Locate every Plasmodium malariae-infected red blood cell.
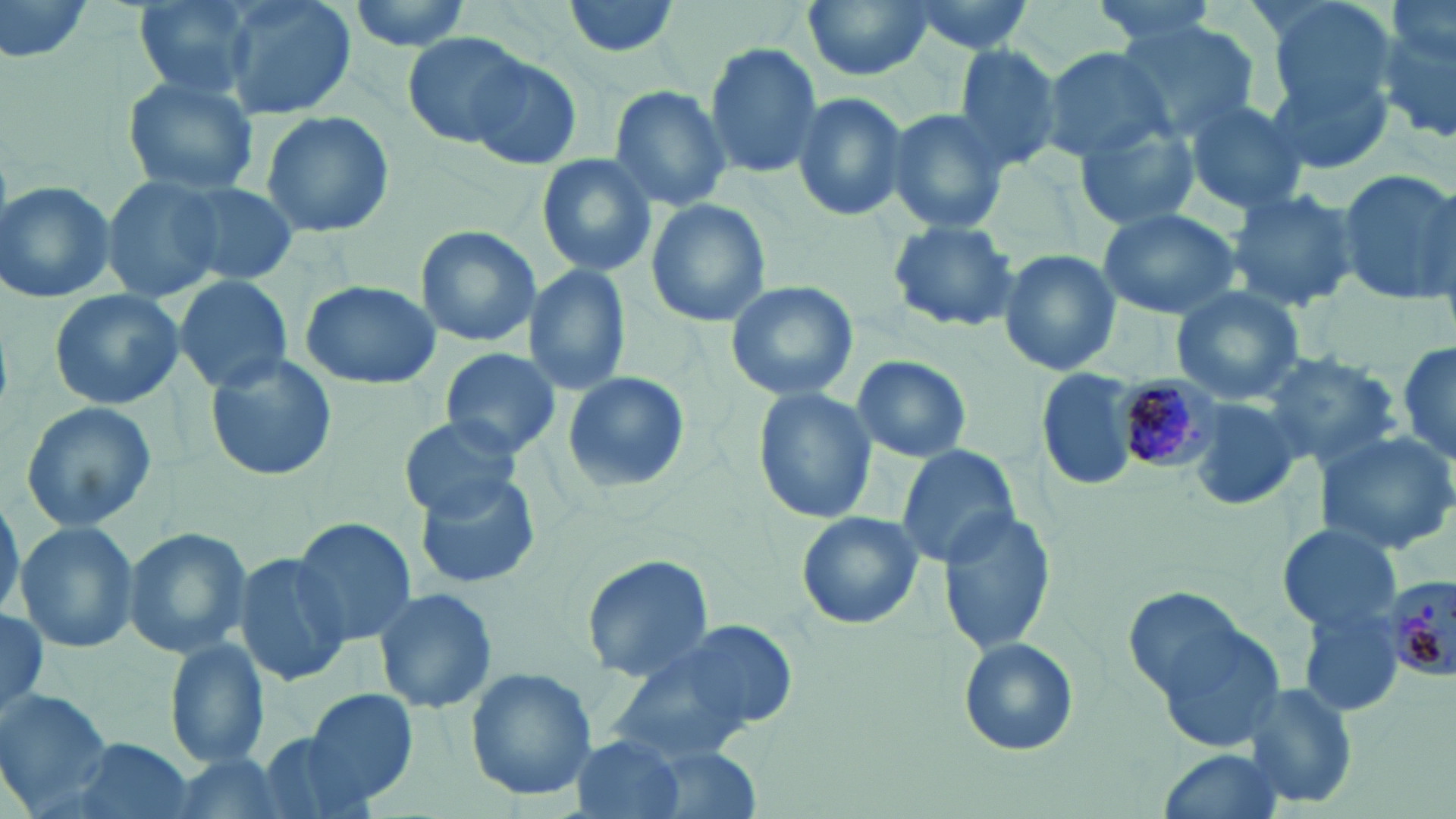

Approximate bounding boxes as named x1/y1/x2/y2 corners in pixels.
Plasmodium malariae-infected red blood cells: (x1=1106, y1=373, x2=1225, y2=472), (x1=1385, y1=575, x2=1456, y2=684).

slide-level diagnosis = Plasmodium malariae
stain = May-Grünwald-Giemsa
modality = optical microscopy
image size = 1456×819 pixels
preparation = thin blood smear
uninfected red blood cell locations = approximate bounding boxes as named x1/y1/x2/y2 corners in pixels: (x1=0, y1=0, x2=106, y2=65), (x1=130, y1=0, x2=257, y2=96), (x1=220, y1=0, x2=355, y2=121), (x1=345, y1=0, x2=479, y2=52), (x1=561, y1=0, x2=685, y2=58), (x1=802, y1=0, x2=935, y2=82), (x1=895, y1=0, x2=1039, y2=57), (x1=1086, y1=0, x2=1224, y2=50), (x1=1377, y1=0, x2=1456, y2=147), (x1=1261, y1=13, x2=1397, y2=173), (x1=1118, y1=21, x2=1261, y2=142), (x1=403, y1=31, x2=529, y2=147), (x1=702, y1=41, x2=825, y2=180), (x1=948, y1=41, x2=1065, y2=176), (x1=1040, y1=46, x2=1175, y2=162), (x1=464, y1=53, x2=585, y2=172), (x1=120, y1=73, x2=262, y2=197), (x1=607, y1=86, x2=732, y2=212), (x1=790, y1=90, x2=910, y2=221), (x1=1181, y1=97, x2=1310, y2=215), (x1=882, y1=106, x2=1012, y2=235), (x1=260, y1=109, x2=395, y2=239), (x1=1074, y1=121, x2=1200, y2=234), (x1=538, y1=152, x2=658, y2=277), (x1=1336, y1=170, x2=1454, y2=304), (x1=99, y1=176, x2=227, y2=301), (x1=170, y1=180, x2=299, y2=286), (x1=1, y1=181, x2=120, y2=304), (x1=1224, y1=187, x2=1361, y2=314), (x1=645, y1=198, x2=770, y2=327), (x1=1096, y1=207, x2=1242, y2=318), (x1=886, y1=219, x2=1021, y2=334), (x1=413, y1=225, x2=542, y2=349), (x1=997, y1=248, x2=1122, y2=377), (x1=522, y1=265, x2=631, y2=395), (x1=172, y1=275, x2=293, y2=392), (x1=724, y1=278, x2=860, y2=403), (x1=298, y1=279, x2=441, y2=390), (x1=1171, y1=286, x2=1307, y2=404), (x1=47, y1=288, x2=186, y2=411), (x1=1397, y1=341, x2=1454, y2=469), (x1=441, y1=347, x2=560, y2=457), (x1=1260, y1=352, x2=1401, y2=468), (x1=205, y1=353, x2=337, y2=482), (x1=847, y1=355, x2=974, y2=464), (x1=1038, y1=367, x2=1139, y2=495), (x1=560, y1=370, x2=691, y2=494), (x1=752, y1=389, x2=876, y2=522), (x1=1187, y1=394, x2=1307, y2=513), (x1=20, y1=400, x2=156, y2=535), (x1=397, y1=415, x2=522, y2=520), (x1=1315, y1=428, x2=1456, y2=555), (x1=895, y1=445, x2=1020, y2=568), (x1=413, y1=469, x2=542, y2=590), (x1=0, y1=493, x2=23, y2=626), (x1=937, y1=508, x2=1057, y2=656), (x1=794, y1=511, x2=924, y2=631), (x1=291, y1=517, x2=416, y2=648), (x1=15, y1=522, x2=140, y2=654), (x1=1278, y1=522, x2=1403, y2=634), (x1=120, y1=526, x2=253, y2=660), (x1=235, y1=553, x2=350, y2=686), (x1=580, y1=554, x2=715, y2=681), (x1=373, y1=585, x2=497, y2=715), (x1=1297, y1=602, x2=1408, y2=717), (x1=0, y1=604, x2=49, y2=719), (x1=1142, y1=605, x2=1289, y2=747), (x1=599, y1=623, x2=787, y2=768), (x1=165, y1=637, x2=272, y2=770), (x1=956, y1=637, x2=1078, y2=756), (x1=465, y1=668, x2=597, y2=801), (x1=1243, y1=682, x2=1360, y2=811), (x1=305, y1=688, x2=424, y2=804), (x1=0, y1=691, x2=112, y2=814), (x1=258, y1=732, x2=375, y2=819), (x1=569, y1=734, x2=690, y2=819), (x1=67, y1=736, x2=195, y2=819), (x1=1155, y1=747, x2=1287, y2=818), (x1=162, y1=753, x2=295, y2=819)
magnification = 1000x
field of view = single